Report the malaria status of this cell.
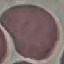
Uninfected.

Photographed with a smartphone camera at the microscope eyepiece. Giemsa stain. Thin blood smear. Cell patch, automatically extracted from a larger field of view and resized to 64 × 64 pixels.